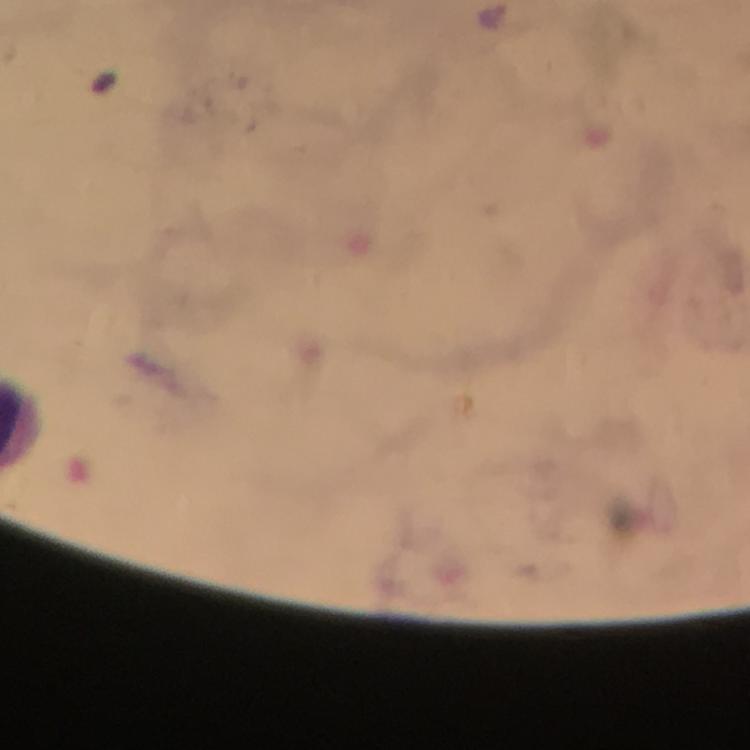 Approximate centers as [x, y] in pixels. Plasmodium parasite locations: [490, 15]. Immersion oil was used. From a diagnostic examination for malaria. Smartphone photograph taken through a microscope. A crop from one field of view. Giemsa-stained preparation. At 100x magnification. Image is 750×750 pixels. Thick smear.